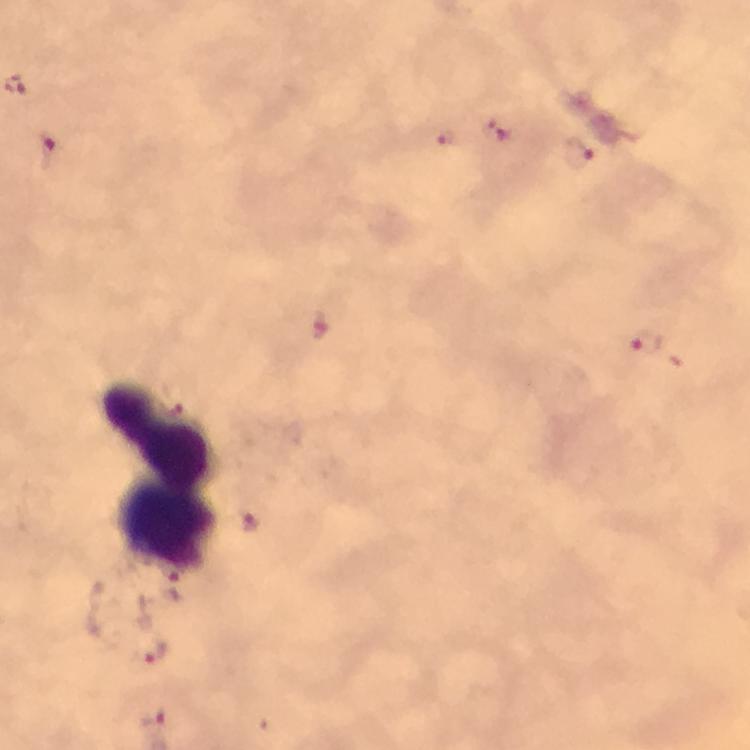
cropped from = one field of view
magnification = 100x
stain = Giemsa
Plasmodium parasite locations = approximate centers as {x, y} in pixels: {16, 87}, {495, 132}, {445, 137}, {48, 152}, {578, 153}, {318, 325}, {649, 341}, {173, 407}, {253, 522}, {166, 573}, {156, 653}, {155, 718}
preparation = thick blood smear
leukocyte locations = approximate centers as {x, y} in pixels: {158, 433}, {169, 523}
context = from a diagnostic examination for malaria
immersion oil = applied
capture = smartphone photograph through a microscope
image size = 750×750 pixels